Describe the morphology of the red blood cells.
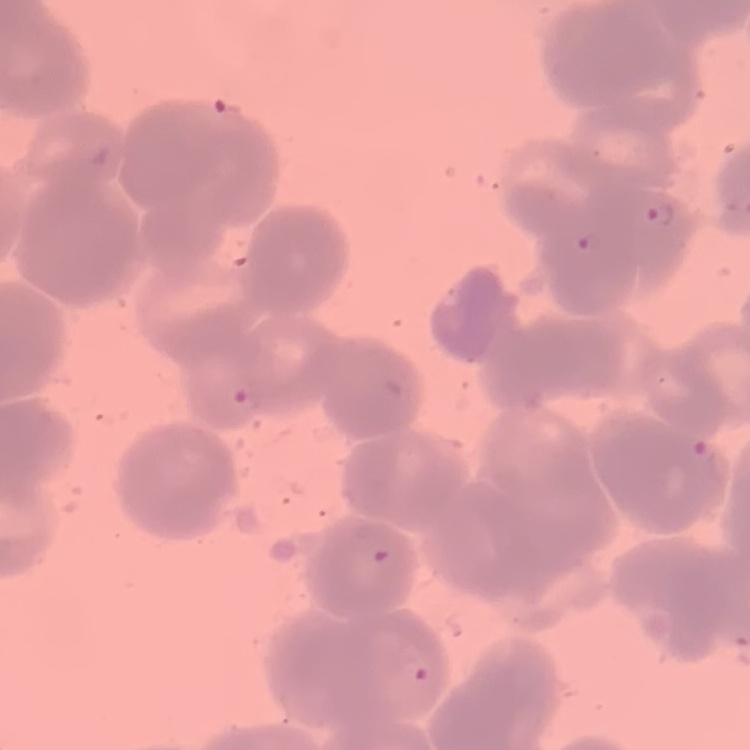

They show rouleaux formation.

{
  "preparation": "thin blood film",
  "stain": "Field's or Giemsa",
  "image_type": "one tile cut from a larger photomicrograph"
}